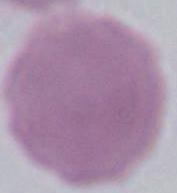
magnification = 1000x
modality = photomicrograph
identification = red blood cell